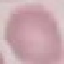 Result: no malaria parasites detected. Photographed with a smartphone camera at the microscope eyepiece. Thin blood smear. Giemsa-stained preparation. Cell patch, automatically extracted from a larger field of view and resized to 64 × 64 pixels.